Comment on the morphology of the erythrocytes.
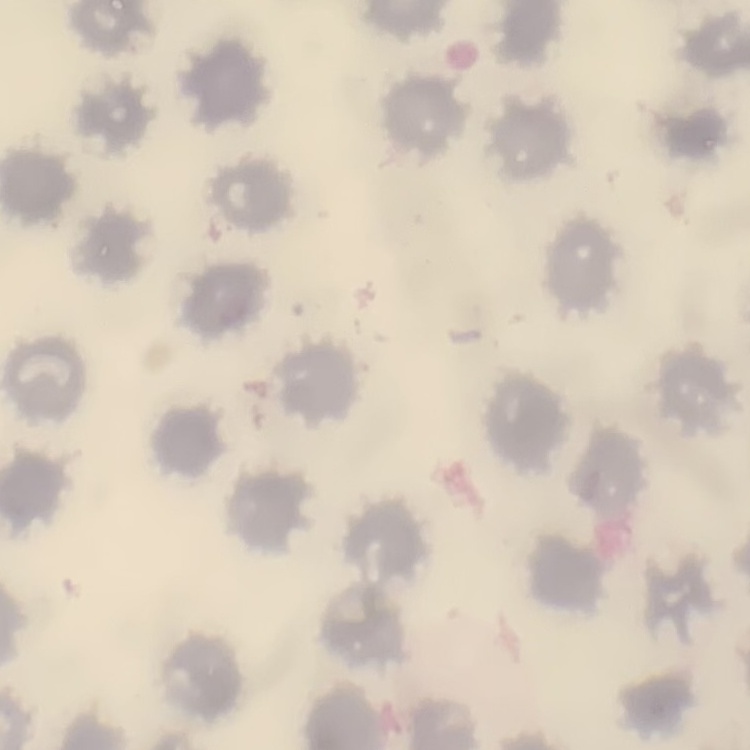

No rouleaux formation.

Summary:
  - Stain: Field's or Giemsa
  - Preparation: thin peripheral smear
  - Image type: one tile cut from a larger photomicrograph